Name the parasite shown.
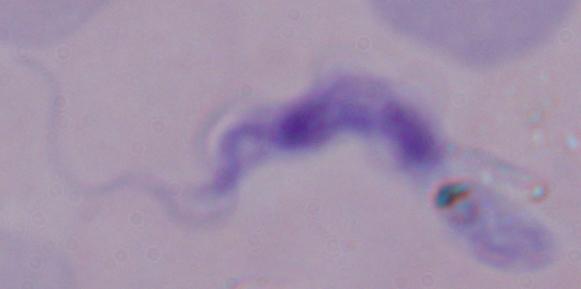

A trypanosome.

Summary:
  - Magnification: 1000x
  - Modality: photomicrograph